Name the cell type shown.
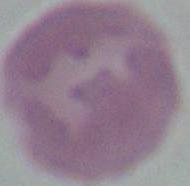
An erythrocyte.

Summary:
  - Magnification: 1000x
  - Modality: micrograph